Report the malaria status of this cell.
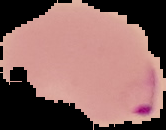
Parasitized.

Image is 166×130 pixels. Segmented cell region on a black background. From a thin blood smear.